Name the parasite shown.
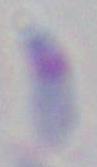
Toxoplasma gondii.

magnification = 1000x
modality = micrograph